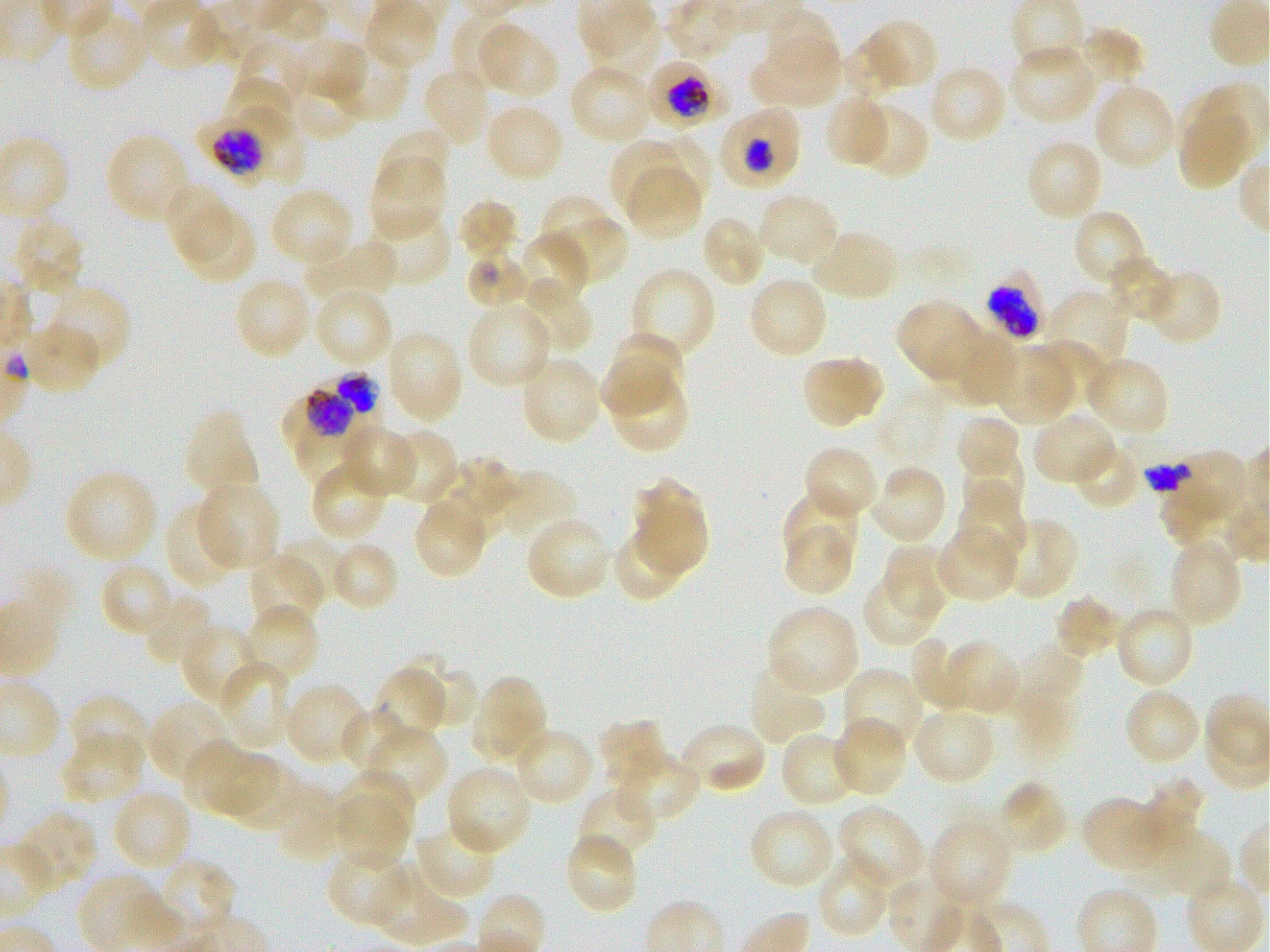
Approximate bounding boxes as {x1, y1, x2, y2} in pixels. Not every red blood cell is marked. A life-cycle stage — or a range of stages, where the recorded stages span more than one — follows each staged infected red blood cell.
Summary:
  - Locations of uninfected red blood cells: {66, 9, 148, 92}, {450, 10, 522, 88}, {761, 17, 840, 88}, {591, 18, 661, 75}, {861, 19, 938, 92}, {479, 22, 558, 98}, {1076, 25, 1146, 86}, {291, 36, 366, 102}, {233, 38, 308, 107}, {750, 38, 840, 110}, {840, 41, 897, 99}, {330, 45, 409, 123}, {1008, 45, 1099, 125}, {568, 63, 652, 144}, {927, 65, 1008, 144}, {421, 66, 493, 147}, {288, 72, 362, 142}, {223, 73, 295, 136}, {1093, 83, 1176, 170}, {824, 95, 890, 169}, {484, 103, 564, 184}, {855, 103, 929, 180}, {1177, 104, 1250, 190}, {375, 126, 450, 198}, {105, 132, 191, 223}, {653, 135, 712, 203}, {609, 139, 688, 218}, {1025, 139, 1105, 222}, {369, 159, 447, 238}, {626, 166, 702, 239}, {162, 182, 234, 261}, {269, 186, 354, 267}, {757, 192, 840, 268}, {458, 199, 518, 263}, {541, 201, 623, 282}, {182, 206, 257, 285}, {368, 208, 452, 288}, {1073, 209, 1150, 290}, {699, 215, 766, 289}, {11, 218, 86, 296}, {810, 229, 900, 302}, {515, 231, 592, 308}, {304, 239, 399, 311}, {1106, 253, 1175, 322}, {631, 265, 717, 361}, {1147, 267, 1223, 347}, {233, 276, 312, 359}, {748, 276, 829, 359}, {518, 278, 594, 355}, {47, 286, 132, 372}, {314, 287, 395, 368}, {1046, 289, 1129, 369}, {894, 298, 983, 383}, {466, 303, 554, 389}, {22, 323, 102, 395}, {939, 329, 1018, 406}, {386, 332, 464, 422}, {611, 333, 686, 400}, {1037, 338, 1106, 407}, {994, 346, 1074, 424}, {802, 356, 883, 429}, {1085, 356, 1171, 438}, {519, 357, 603, 445}, {596, 358, 673, 414}, {615, 378, 690, 454}, {182, 410, 259, 497}, {955, 413, 1020, 482}, {1032, 413, 1117, 487}, {341, 422, 417, 499}, {387, 429, 459, 506}, {295, 430, 369, 484}, {1072, 438, 1142, 511}, {802, 445, 879, 522}, {960, 452, 1025, 519}, {435, 456, 521, 531}, {309, 460, 389, 542}, {868, 465, 948, 545}, {63, 469, 159, 564}, {497, 471, 579, 546}, {632, 477, 708, 573}, {196, 479, 280, 571}, {953, 487, 1026, 567}, {1159, 487, 1232, 548}, {782, 490, 858, 567}, {413, 498, 488, 580}, {163, 503, 237, 591}, {524, 515, 612, 601}, {998, 516, 1078, 601}, {783, 524, 855, 596}, {611, 525, 688, 603}, {936, 526, 1020, 603}, {277, 534, 349, 601}, {1167, 538, 1244, 630}, {329, 541, 400, 614}, {881, 545, 951, 618}, {248, 553, 324, 631}, {99, 562, 174, 639}, {861, 572, 941, 647}, {142, 592, 217, 666}, {1052, 594, 1121, 661}, {243, 603, 320, 684}, {766, 604, 860, 697}, {1115, 605, 1195, 689}, {180, 623, 262, 707}, {909, 638, 974, 713}, {942, 640, 1020, 717}, {1008, 644, 1085, 719}, {403, 650, 477, 728}, {218, 660, 294, 751}, {748, 663, 826, 747}, {375, 666, 447, 741}, {841, 667, 922, 754}, {477, 677, 543, 755}, {284, 683, 368, 766}, {1123, 688, 1201, 767}, {67, 695, 149, 769}, {147, 700, 232, 784}, {339, 707, 410, 778}, {910, 708, 996, 786}, {470, 713, 547, 763}, {596, 717, 667, 791}, {832, 717, 907, 797}, {366, 725, 448, 806}, {681, 726, 766, 792}, {518, 731, 593, 802}, {780, 731, 860, 808}, {61, 733, 146, 805}, {182, 740, 245, 811}, {206, 749, 278, 816}, {616, 749, 702, 823}, {223, 758, 302, 831}, {444, 764, 533, 857}, {335, 769, 414, 847}, {1144, 777, 1205, 846}, {999, 780, 1070, 857}, {577, 787, 659, 865}, {112, 788, 193, 872}, {275, 789, 344, 863}, {335, 792, 410, 874}, {1080, 796, 1166, 872}, {837, 805, 926, 891}, {748, 808, 836, 891}, {17, 810, 98, 892}, {928, 818, 1012, 911}, {414, 821, 497, 900}, {1149, 829, 1232, 896}, {567, 837, 634, 911}, {329, 851, 411, 925}, {815, 854, 890, 939}, {157, 857, 236, 937}, {373, 865, 469, 946}
  - Locations of infected red blood cells: {645, 59, 726, 131} early trophozoite to early schizont; {719, 104, 804, 191} early trophozoite to early schizont; {196, 117, 272, 190} early trophozoite to early schizont; {984, 270, 1047, 342}; {304, 373, 379, 435}; {283, 391, 363, 450} trophozoite
  - Locations of red blood cells of indeterminate infection status: {236, 107, 308, 185}, {464, 251, 531, 309}, {1158, 454, 1248, 511}
  - Stain: Giemsa
  - Image size: 1270×952 pixels
  - Donor blood group: O+
  - Preparation: thin blood film
  - Field of view: single
  - Objective: 100x, oil immersion, numerical aperture 1.25
  - Culture: static in-vitro P. falciparum strain 3D7